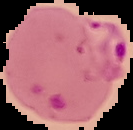

Summary:
  - Image type: cell region segmented out of the field of view; surrounding area masked to black
  - Malaria status: parasitized
  - Image size: 133×130 pixels
  - Preparation: thin blood smear